Classify this cell by malaria status.
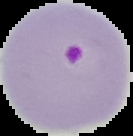
Parasitized.

image type = segmented cell region on a black background
image size = 133×136 pixels
preparation = thin blood smear